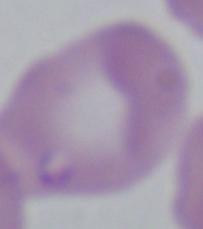

Photomicrograph. A Babesia parasite is seen. Captured at 1000x magnification.